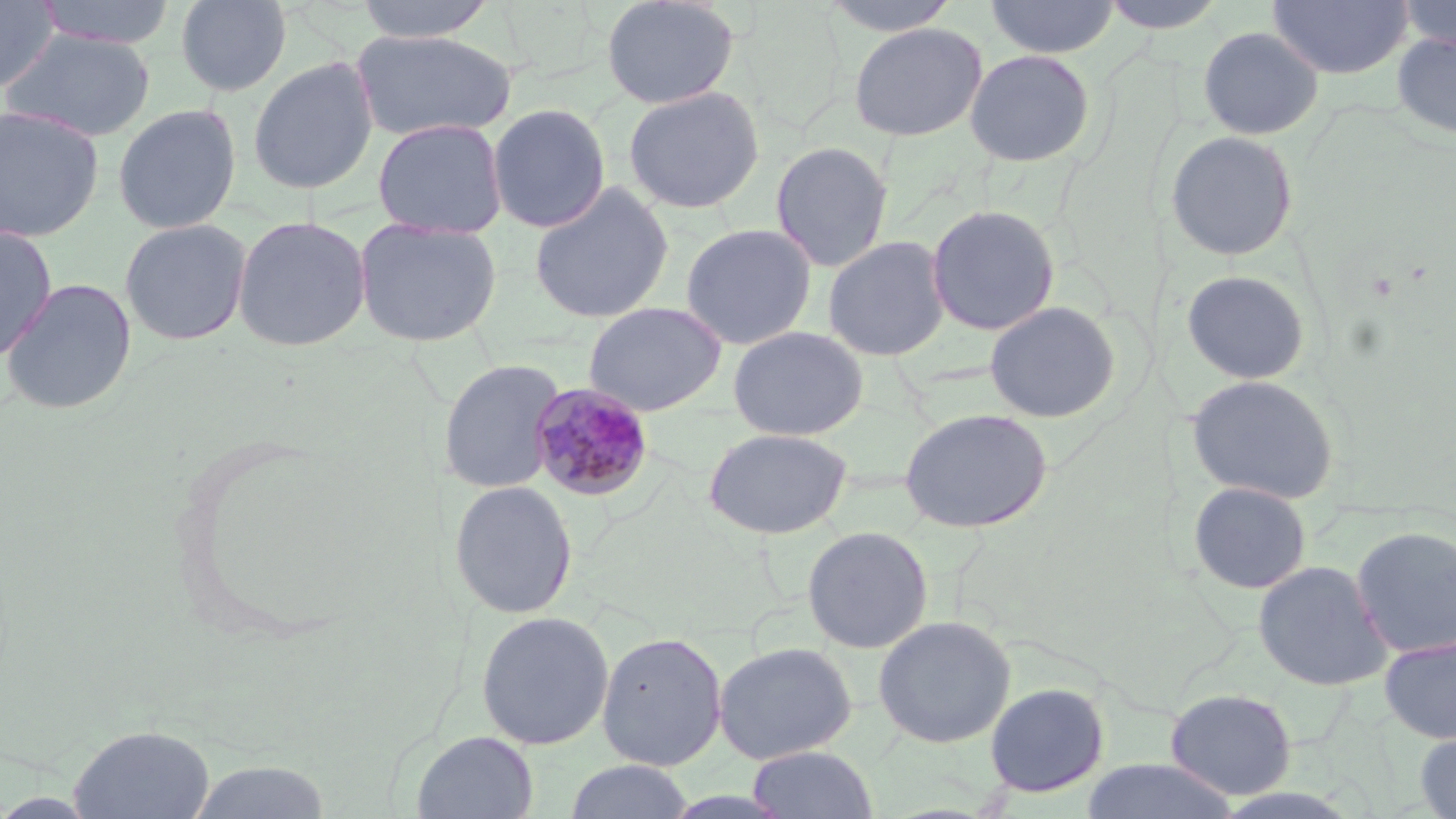 Approximate bounding boxes as (x1,y1)-(x2,y2) corner pairs in pixels. Uninfected red blood cell locations: (32,0)-(178,49), (175,0)-(292,97), (352,0)-(500,42), (600,0)-(740,110), (819,0)-(964,37), (984,0)-(1120,59), (1096,0)-(1230,34), (1267,0)-(1413,80), (1394,0)-(1456,54), (0,1)-(59,94), (848,22)-(988,142), (1197,26)-(1324,140), (0,28)-(156,142), (350,28)-(516,142), (1391,31)-(1456,140), (964,48)-(1095,168), (247,56)-(379,195), (623,85)-(765,214), (112,103)-(241,234), (487,103)-(611,233), (0,105)-(104,243), (372,118)-(508,239), (1164,130)-(1299,262), (770,140)-(893,272), (528,182)-(675,324), (925,203)-(1061,336), (232,214)-(371,352), (353,216)-(503,347), (119,218)-(252,346), (679,222)-(818,350), (0,226)-(58,362), (822,235)-(950,362), (1180,268)-(1312,385), (1,278)-(137,415), (983,300)-(1121,423), (582,301)-(728,416), (727,325)-(869,441), (438,359)-(566,494), (1185,373)-(1340,505), (899,407)-(1054,533), (703,427)-(853,540), (447,480)-(579,619), (1186,480)-(1313,596), (802,525)-(934,654), (1351,525)-(1456,658), (1253,559)-(1392,691), (475,610)-(614,751), (872,614)-(1017,749), (595,630)-(728,771), (1379,634)-(1456,745), (712,641)-(857,764), (983,682)-(1110,798), (1164,688)-(1296,800), (68,723)-(216,819), (412,730)-(539,819), (1413,730)-(1456,819), (746,745)-(879,818), (1079,758)-(1243,818), (185,760)-(332,819), (563,760)-(696,819). Plasmodium malariae-infected red blood cell locations: (529,381)-(656,503). Slide-level diagnosis: Plasmodium malariae. Light microscopy. Image is 1456×819 pixels. Captured at 1000x magnification. Single field of view. May-Grünwald-Giemsa-stained preparation. Thin blood smear.